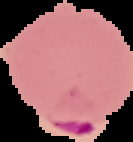

result: Plasmodium parasites detected
image_size: 133×142 pixels
preparation: thin blood smear
image_type: segmented cell region on a black background